Point out each leukocyte.
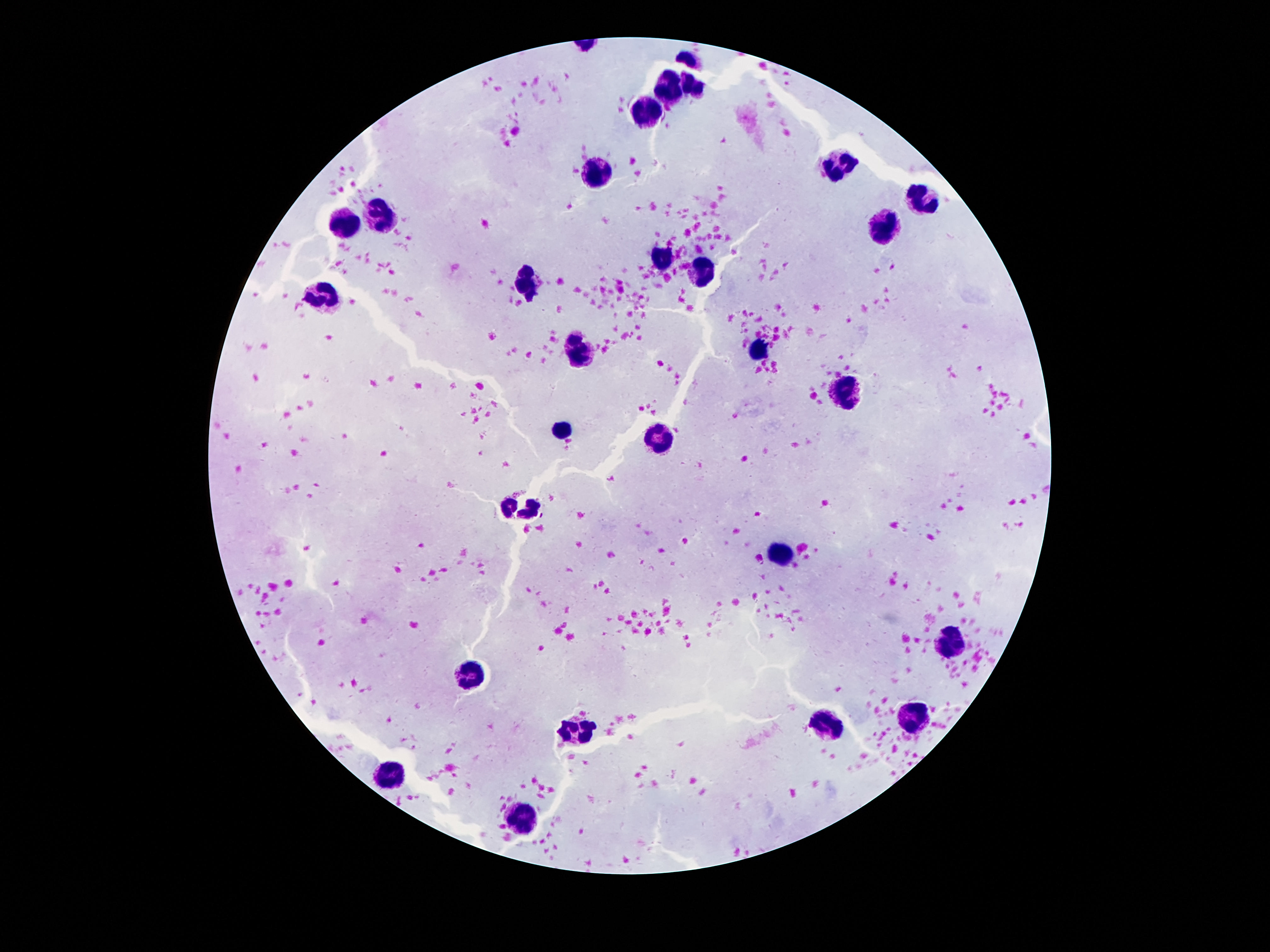

Approximate centers as {x, y} in pixels.
Leukocytes: {667, 93}, {643, 109}, {848, 165}, {602, 174}, {925, 202}, {380, 217}, {348, 226}, {886, 234}, {658, 258}, {699, 275}, {527, 282}, {327, 295}, {761, 351}, {579, 353}, {841, 393}, {561, 426}, {658, 441}, {781, 552}, {951, 643}, {471, 675}, {912, 717}, {830, 724}, {574, 730}, {393, 775}, {525, 816}.

field of view = single
capture = smartphone camera through the microscope eyepiece
stain = Giemsa
patient malaria status = negative
image size = 1270×952 pixels
preparation = thick blood smear
magnification = 100x